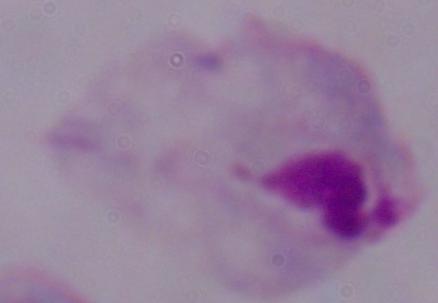

Summary:
  - Identification: trichomonad
  - Magnification: 1000x
  - Modality: photomicrograph